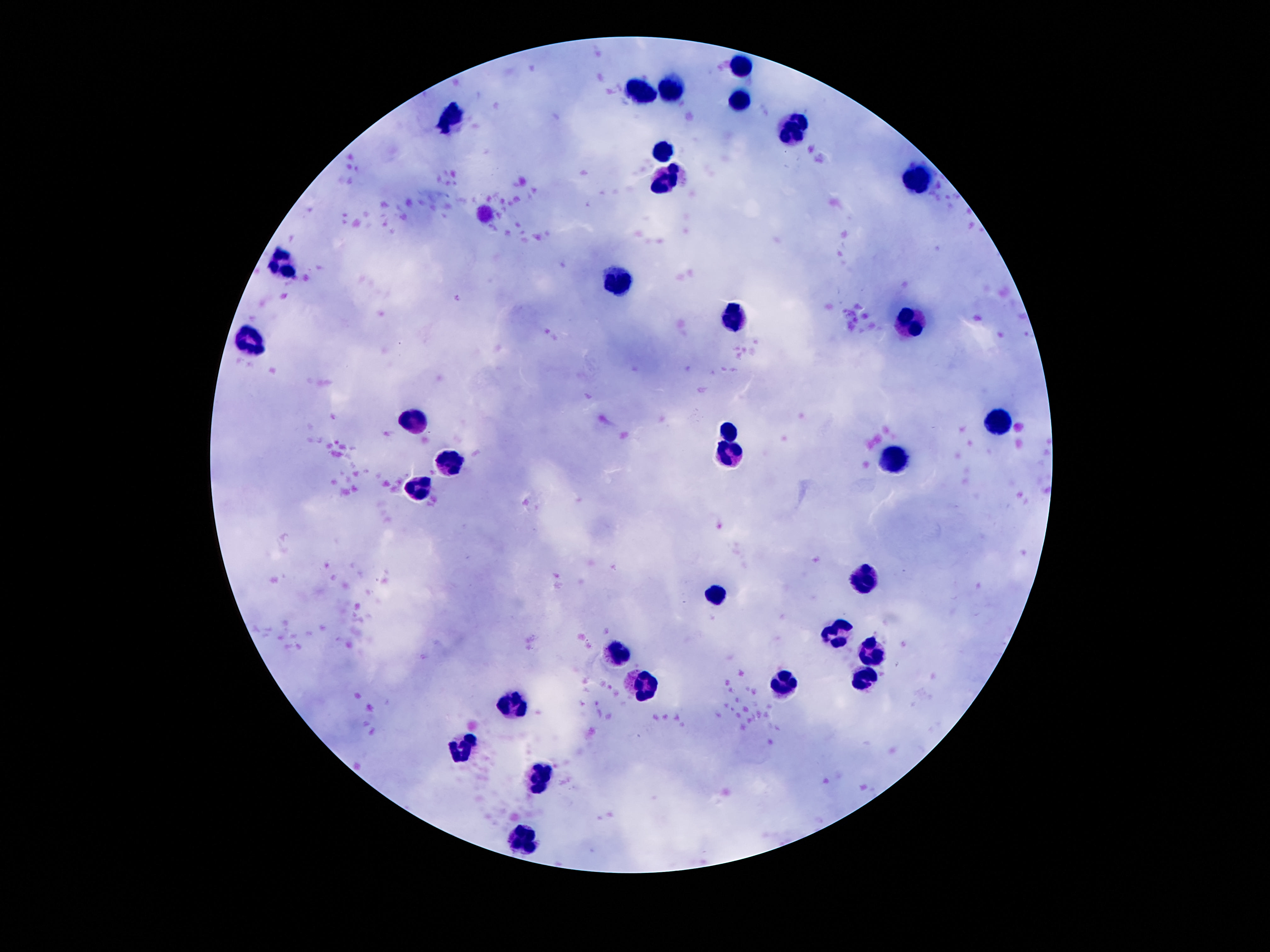

Approximate object centers, in pixels from the top-left corner.
Summary:
  - Leukocyte locations: (x=742, y=66), (x=673, y=90), (x=643, y=92), (x=742, y=101), (x=454, y=116), (x=796, y=130), (x=664, y=152), (x=915, y=180), (x=666, y=183), (x=283, y=262), (x=621, y=276), (x=737, y=316), (x=910, y=323), (x=253, y=343), (x=412, y=417), (x=997, y=421), (x=730, y=429), (x=728, y=452), (x=895, y=457), (x=454, y=460), (x=417, y=489), (x=864, y=577), (x=717, y=595), (x=838, y=631), (x=619, y=652), (x=870, y=652), (x=864, y=678), (x=784, y=680), (x=644, y=690), (x=512, y=709), (x=463, y=750), (x=537, y=778), (x=527, y=838)
  - Field of view: single
  - Magnification: 100x
  - Image size: 1270×952 pixels
  - Capture: smartphone camera through the microscope eyepiece
  - Preparation: thick blood smear
  - Patient malaria status: uninfected
  - Stain: Giemsa